State which parasite is depicted.
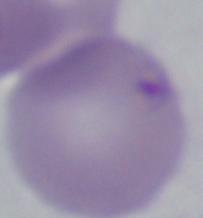
This is Babesia.

Summary:
  - Modality: micrograph
  - Magnification: 1000x